Report the malaria status of this cell.
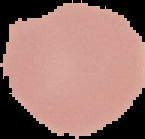
It is uninfected.

Summary:
  - Image size: 145×139 pixels
  - Preparation: thin blood smear
  - Image type: segmented cell region with the area outside set to black